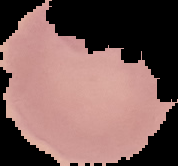
image type = segmented cell region on a black background
malaria status = uninfected
image size = 178×166 pixels
preparation = thin blood smear